Comment on the morphology of the erythrocytes.
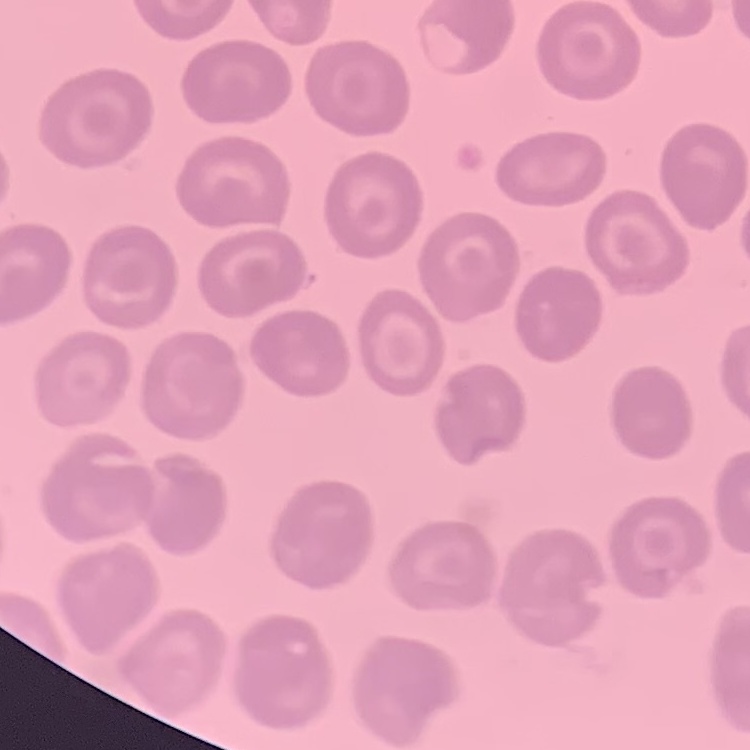

They show no rouleaux formation.

Summary:
  - Image type: one tile cut from a larger photomicrograph
  - Preparation: thin blood film
  - Stain: Field's or Giemsa